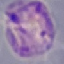
result = malaria parasites identified
capture = smartphone camera at the microscope eyepiece
preparation = thin blood smear
image type = cell patch, automatically extracted from a larger field of view and resized to 64 × 64 pixels
stain = Giemsa